Name the parasite shown.
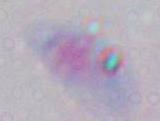
Toxoplasma gondii.

Summary:
  - Modality: photomicrograph
  - Magnification: 1000x